State which parasite is depicted.
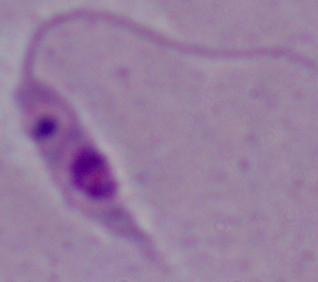

Leishmania.

modality = micrograph
magnification = 1000x